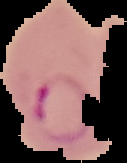
Summary:
  - Result: malaria parasites detected
  - Preparation: thin blood film
  - Image size: 127×163 pixels
  - Image type: cell region segmented out of the field of view; surrounding area masked to black